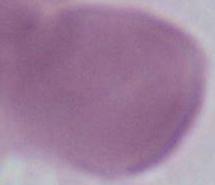

magnification = 1000x
identification = erythrocyte
modality = photomicrograph